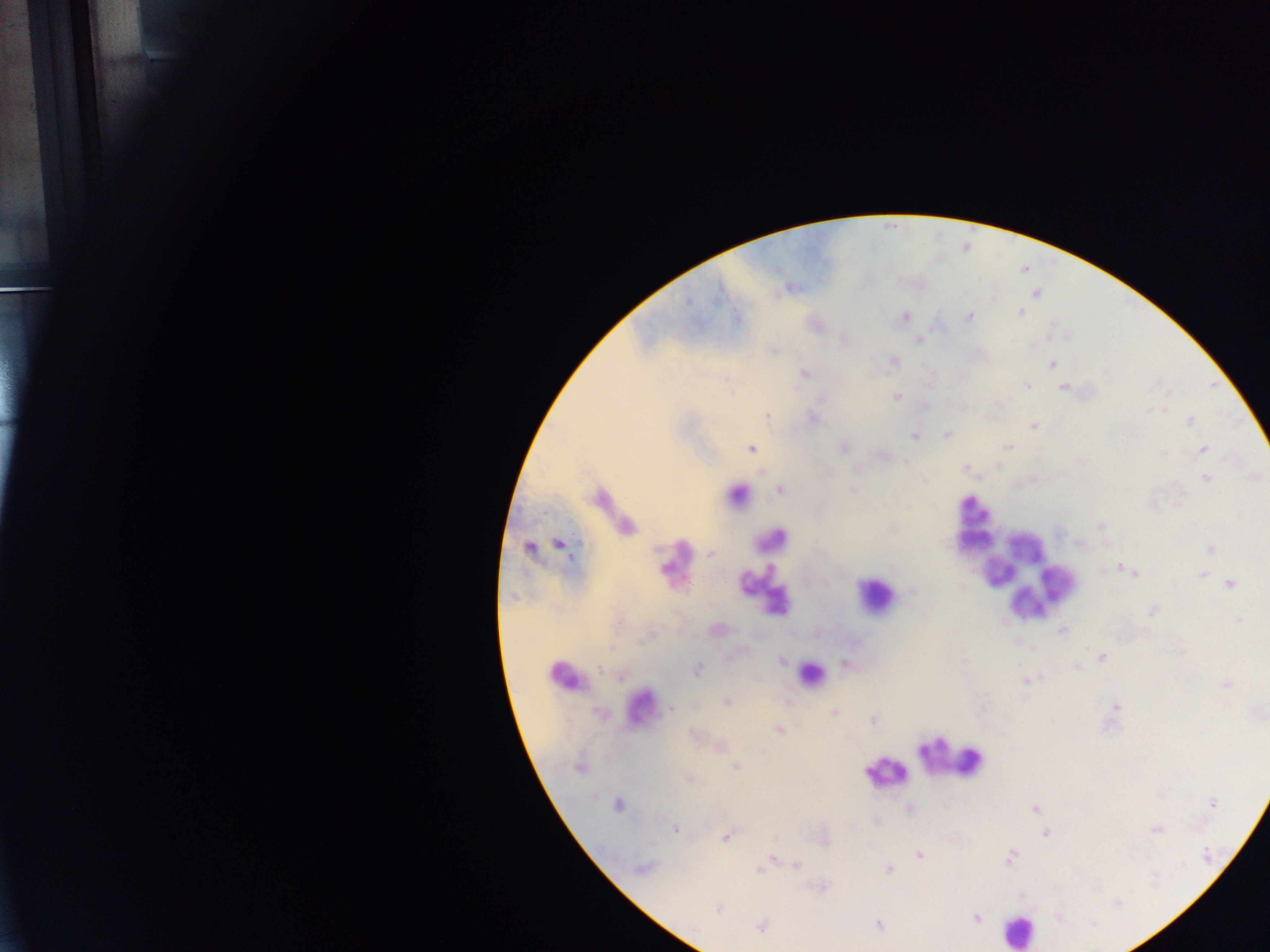

country = Ghana
preparation = thick blood smear
field of view = single
image size = 1270×952 pixels
capture = mobile-phone photograph through a microscope
leukocyte locations = approximate centers as x y in pixels: 736 487; 973 508; 610 512; 975 541; 768 544; 1024 547; 671 558; 998 572; 1022 576; 767 590; 874 594; 809 673; 564 674; 642 701; 951 758; 884 774; 1017 931
Plasmodium parasite locations = approximate centers as x y in pixels: 1036 293; 688 301; 1020 312; 905 316; 970 316; 918 340; 774 350; 893 361; 1052 364; 805 373; 1027 386; 1063 388; 897 397; 767 415; 813 418; 1190 421; 1033 427; 947 434; 914 436; 1008 446; 751 448; 844 448; 1203 449; 1164 454; 906 462; 998 467; 966 468; 1207 478; 780 490; 853 490; 1101 526; 560 544; 528 547; 1210 548; 716 561; 1125 569; 1133 574; 1202 574; 1230 584; 911 592; 1151 611; 1240 620; 1062 630; 1101 657; 782 661; 1077 668; 698 669; 600 671; 1027 681; 1227 683; 727 702; 1116 706; 671 709; 600 713; 835 713; 873 720; 779 731; 721 745; 736 766; 579 767; 688 777; 1213 803; 618 805; 1035 809; 909 810; 876 822; 676 829; 1157 830; 1046 833; 727 838; 920 856; 773 858; 1010 858; 797 865; 642 867; 759 869; 889 869; 717 908; 977 918; 1059 918; 878 924; 761 927